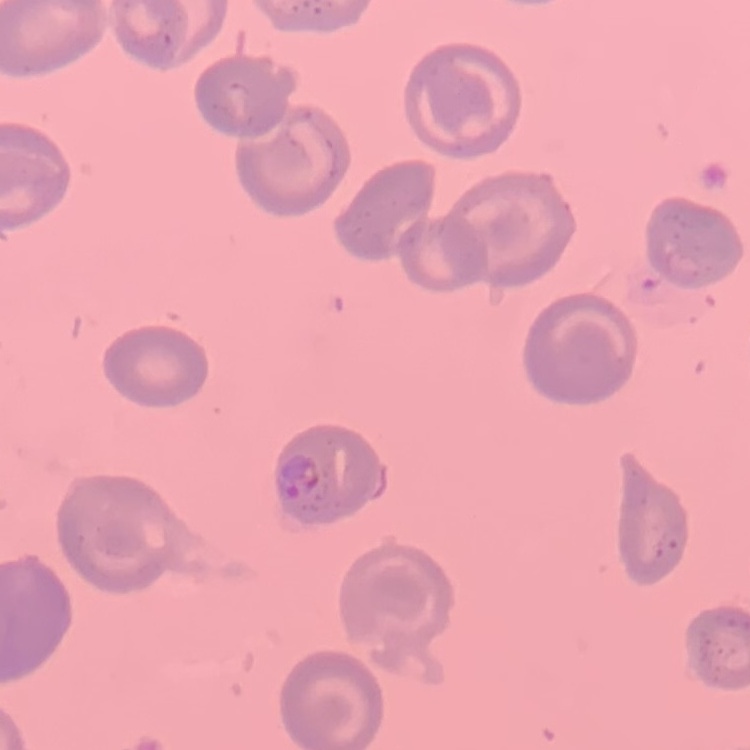
erythrocyte morphology = no rouleaux formation
stain = Field's or Giemsa
preparation = thin blood smear
image type = square crop of a larger photomicrograph